Point out every Plasmodium parasite and every leukocyte.
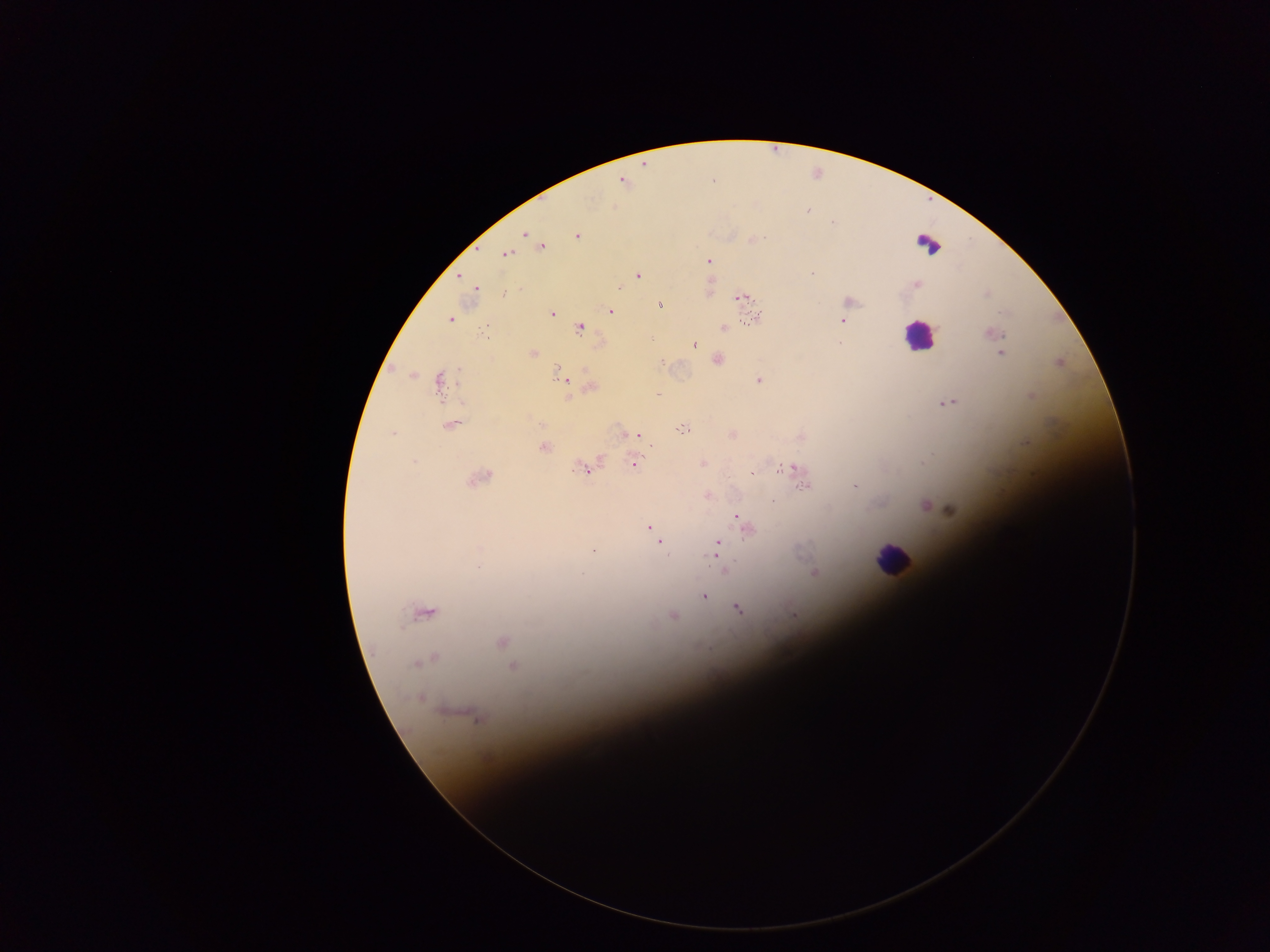

Approximate centers as [x, y] in pixels.
Plasmodium parasites: [621, 182], [807, 211], [833, 222], [524, 234], [578, 237], [542, 246], [506, 253], [709, 260], [812, 273], [637, 275], [460, 276], [917, 283], [620, 288], [476, 289], [987, 293], [503, 294], [742, 296], [850, 301], [659, 306], [611, 310], [1000, 311], [552, 313], [450, 319], [753, 320], [843, 320], [579, 327], [724, 327], [994, 333], [838, 343], [694, 346], [1002, 353], [532, 354], [718, 359], [414, 374], [560, 376], [759, 380], [440, 384], [590, 386], [948, 403], [451, 425], [682, 430], [393, 433], [635, 436], [543, 447], [414, 461], [702, 463], [634, 464], [791, 468], [584, 469], [752, 473], [478, 479], [804, 486], [855, 486], [771, 500], [924, 505], [951, 510], [737, 516], [650, 528], [747, 530], [658, 540], [718, 543], [479, 549], [593, 549], [719, 561], [724, 567], [814, 572], [582, 575], [704, 596], [738, 608], [425, 613], [794, 614], [673, 616], [503, 641], [429, 659], [419, 661], [513, 667], [420, 698], [471, 715].
Leukocytes: [925, 246], [919, 336], [891, 559].

Collected in Ghana. One field of view. Thick blood smear. Image is 1270×952 pixels. Mobile-phone photograph taken through the microscope.